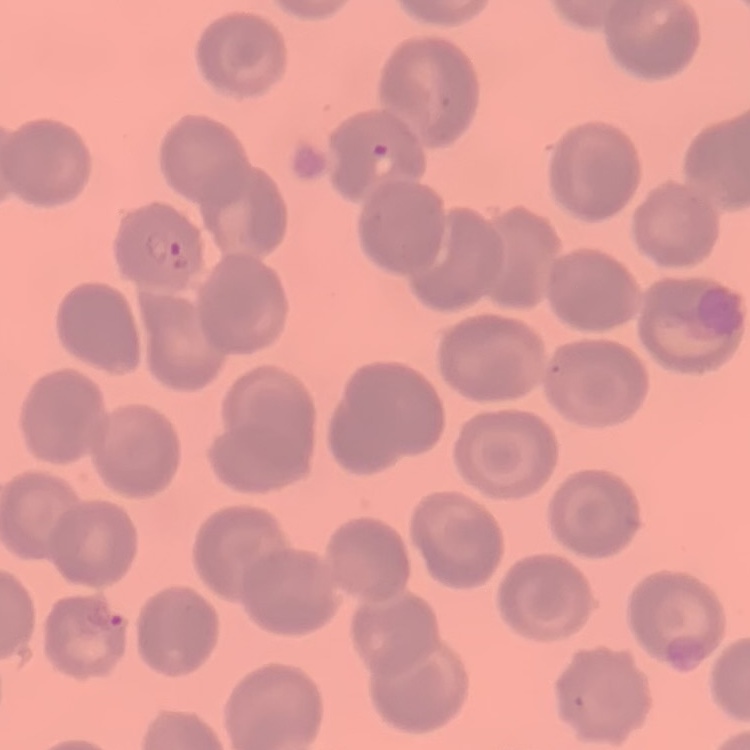
red blood cell morphology = no rouleaux formation
preparation = thin peripheral smear
stain = Field's or Giemsa
image type = one tile cut from a larger photomicrograph